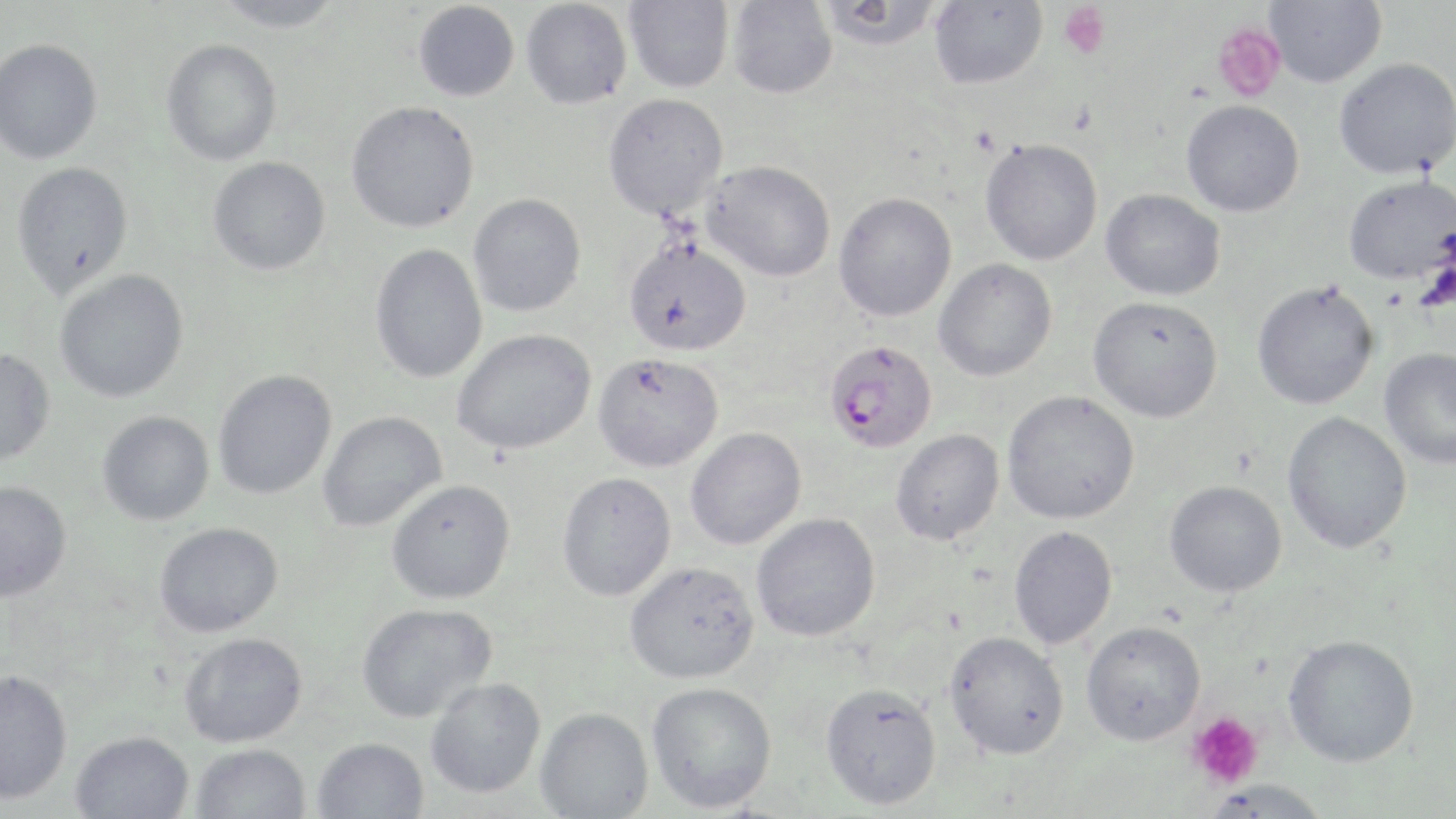
slide-level diagnosis = Plasmodium falciparum
stain = May-Grünwald-Giemsa
image size = 1456×819 pixels
platelet locations = approximate bounding boxes as named x1/y1/x2/y2 corners in pixels: (x1=1058, y1=3, x2=1111, y2=58), (x1=1211, y1=22, x2=1286, y2=103), (x1=1188, y1=711, x2=1265, y2=789)
modality = optical microscopy
uninfected red blood cell locations = approximate bounding boxes as named x1/y1/x2/y2 corners in pixels: (x1=208, y1=0, x2=345, y2=32), (x1=624, y1=0, x2=734, y2=93), (x1=1263, y1=0, x2=1387, y2=88), (x1=413, y1=1, x2=520, y2=101), (x1=521, y1=1, x2=632, y2=110), (x1=727, y1=1, x2=837, y2=99), (x1=817, y1=1, x2=943, y2=52), (x1=929, y1=1, x2=1047, y2=89), (x1=0, y1=38, x2=103, y2=165), (x1=161, y1=39, x2=283, y2=166), (x1=1334, y1=58, x2=1456, y2=180), (x1=603, y1=92, x2=729, y2=220), (x1=346, y1=100, x2=480, y2=233), (x1=1181, y1=100, x2=1305, y2=217), (x1=980, y1=138, x2=1103, y2=265), (x1=207, y1=156, x2=331, y2=276), (x1=701, y1=159, x2=836, y2=282), (x1=11, y1=161, x2=134, y2=298), (x1=1343, y1=175, x2=1455, y2=286), (x1=1100, y1=188, x2=1225, y2=301), (x1=834, y1=192, x2=957, y2=321), (x1=468, y1=193, x2=586, y2=317), (x1=623, y1=236, x2=752, y2=356), (x1=369, y1=243, x2=487, y2=384), (x1=933, y1=258, x2=1057, y2=382), (x1=55, y1=269, x2=189, y2=403), (x1=1252, y1=282, x2=1378, y2=410), (x1=1087, y1=295, x2=1223, y2=422), (x1=452, y1=328, x2=596, y2=455), (x1=0, y1=347, x2=56, y2=466), (x1=1379, y1=348, x2=1455, y2=468), (x1=593, y1=353, x2=725, y2=473), (x1=213, y1=369, x2=337, y2=499), (x1=1001, y1=390, x2=1140, y2=524), (x1=97, y1=411, x2=214, y2=525), (x1=317, y1=411, x2=447, y2=531), (x1=1282, y1=412, x2=1412, y2=554), (x1=685, y1=427, x2=806, y2=550), (x1=890, y1=429, x2=1005, y2=546), (x1=556, y1=471, x2=677, y2=601), (x1=386, y1=479, x2=515, y2=605), (x1=1164, y1=480, x2=1287, y2=597), (x1=0, y1=481, x2=71, y2=602), (x1=751, y1=512, x2=880, y2=642), (x1=154, y1=522, x2=283, y2=637), (x1=1008, y1=525, x2=1118, y2=649), (x1=624, y1=561, x2=760, y2=684), (x1=356, y1=602, x2=497, y2=723), (x1=1081, y1=621, x2=1206, y2=745), (x1=944, y1=631, x2=1069, y2=759), (x1=180, y1=632, x2=308, y2=747), (x1=1282, y1=634, x2=1420, y2=768), (x1=0, y1=669, x2=73, y2=805), (x1=425, y1=678, x2=546, y2=799), (x1=647, y1=682, x2=777, y2=813), (x1=820, y1=683, x2=942, y2=810), (x1=534, y1=707, x2=654, y2=818), (x1=70, y1=730, x2=194, y2=819), (x1=313, y1=737, x2=429, y2=819), (x1=191, y1=743, x2=311, y2=819), (x1=1203, y1=779, x2=1334, y2=818)
magnification = 1000x
field of view = single
Plasmodium falciparum-infected red blood cell locations = approximate bounding boxes as named x1/y1/x2/y2 corners in pixels: (x1=824, y1=340, x2=937, y2=452)
preparation = thin blood film